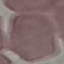

result: no malaria parasites detected
preparation: thin blood smear
stain: Giemsa
capture: smartphone camera at the microscope eyepiece
image_type: automatically extracted cell patch, resized to 64 × 64 pixels